Comment on the morphology of the red blood cells.
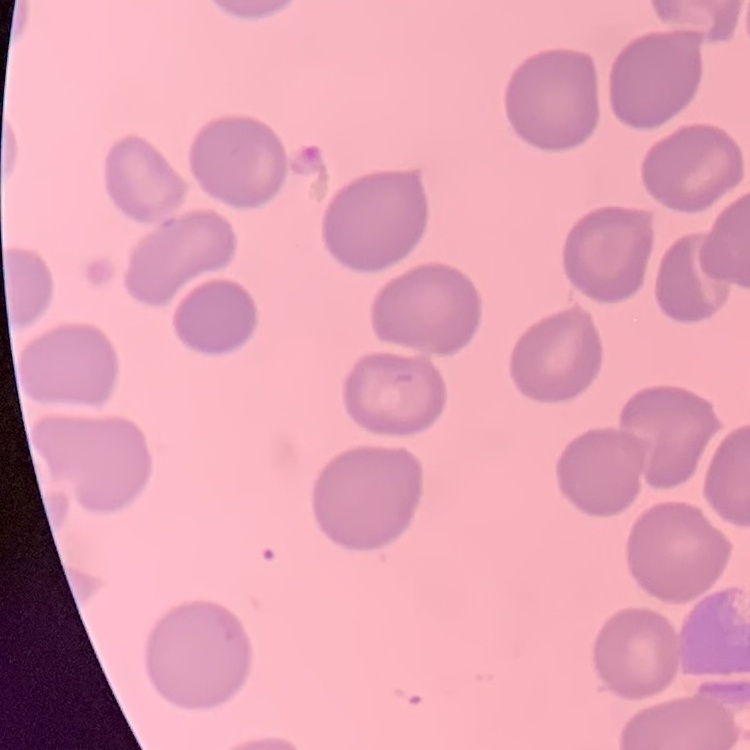

They show no rouleaux formation.

{
  "stain": "Field's or Giemsa",
  "image_type": "square crop of a larger photomicrograph",
  "preparation": "thin peripheral smear"
}